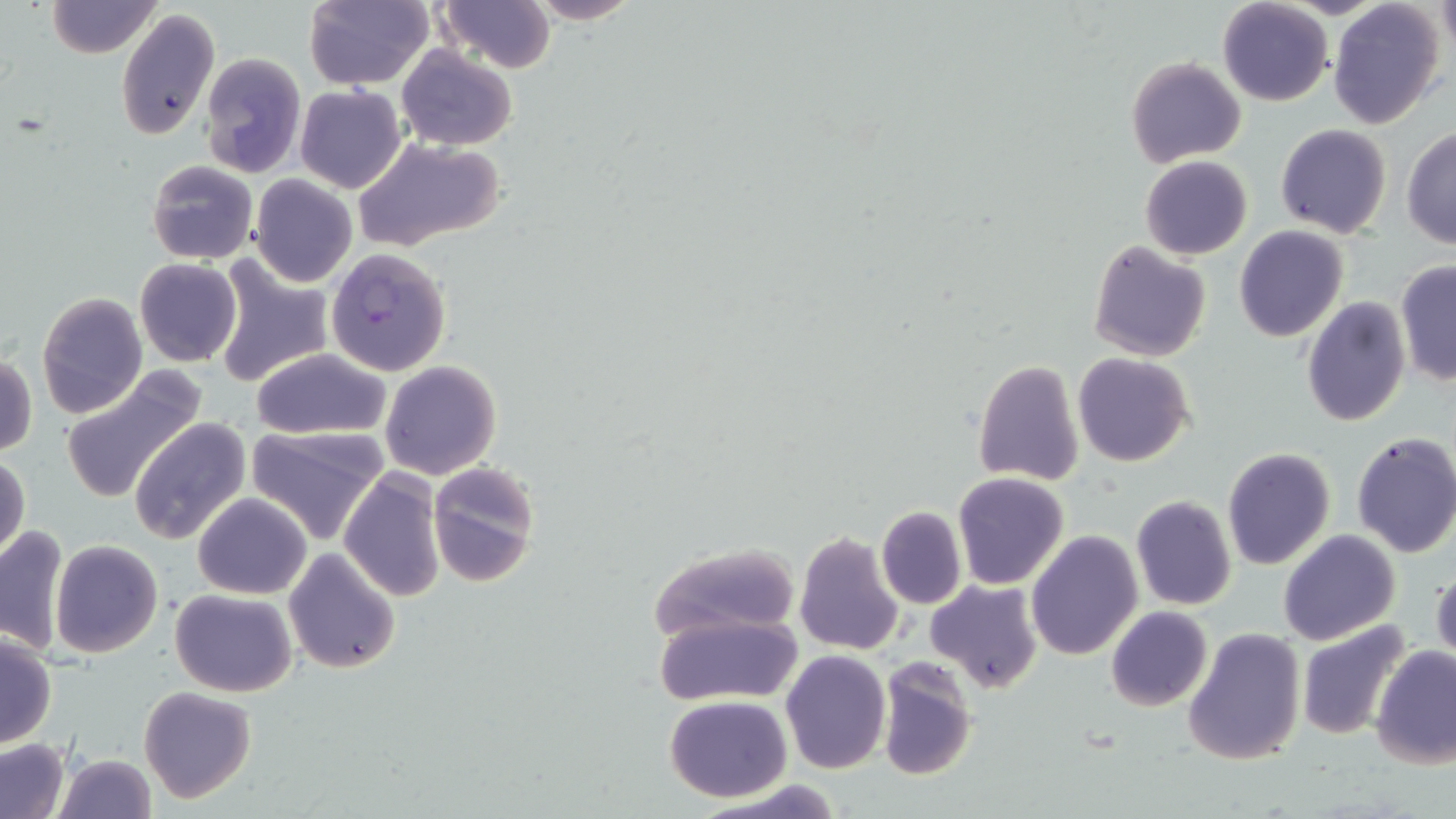

Approximate bounding boxes as [x1, y1, x2, y2] in pixels. Plasmodium falciparum-infected red blood cell locations: [325, 247, 451, 376]. Uninfected red blood cell locations: [47, 0, 161, 57], [305, 0, 434, 90], [527, 0, 641, 24], [1328, 0, 1447, 130], [438, 1, 555, 72], [1217, 1, 1333, 106], [116, 7, 220, 141], [397, 45, 517, 151], [199, 51, 306, 178], [1126, 56, 1246, 169], [295, 84, 406, 193], [1275, 123, 1392, 238], [1400, 127, 1456, 248], [353, 138, 506, 255], [1140, 155, 1253, 259], [146, 159, 258, 265], [249, 175, 359, 288], [1234, 226, 1349, 343], [1088, 239, 1211, 362], [135, 258, 242, 367], [212, 258, 334, 389], [1394, 262, 1456, 386], [36, 292, 148, 419], [1301, 297, 1411, 428], [251, 347, 392, 441], [1, 352, 37, 459], [1073, 353, 1195, 468], [380, 360, 502, 480], [972, 360, 1086, 486], [57, 369, 207, 503], [129, 415, 253, 544], [246, 426, 387, 544], [1350, 430, 1456, 557], [1224, 443, 1456, 565], [1222, 446, 1335, 570], [1, 453, 29, 563], [426, 462, 541, 586], [338, 468, 444, 604], [952, 472, 1068, 589], [192, 491, 311, 599], [1129, 496, 1237, 611], [875, 506, 967, 610], [0, 524, 69, 656], [1279, 529, 1400, 645], [793, 530, 906, 657], [1026, 531, 1143, 661], [49, 540, 162, 657], [648, 542, 804, 642], [284, 547, 400, 673], [1431, 565, 1455, 670], [925, 579, 1044, 694], [170, 587, 297, 696], [1104, 607, 1212, 711], [654, 613, 803, 705], [1297, 619, 1413, 740], [1182, 625, 1307, 767], [0, 633, 56, 748], [1370, 645, 1456, 769], [780, 649, 891, 773], [875, 659, 978, 782], [138, 686, 255, 803], [665, 696, 793, 802], [0, 740, 70, 819], [53, 753, 157, 819]. Slide-level diagnosis: Plasmodium falciparum. Thin blood film. Image is 1456×819 pixels. May-Grünwald-Giemsa-stained preparation. Optical microscopy. Single field of view. 1000x magnification.